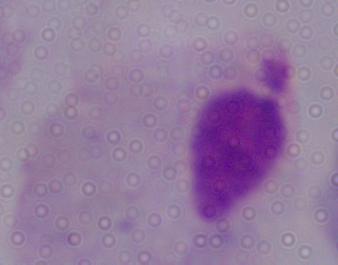

identification = trichomonad
modality = micrograph
magnification = 1000x